Name the parasite shown.
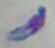

This is Toxoplasma gondii.

modality = photomicrograph
magnification = 1000x